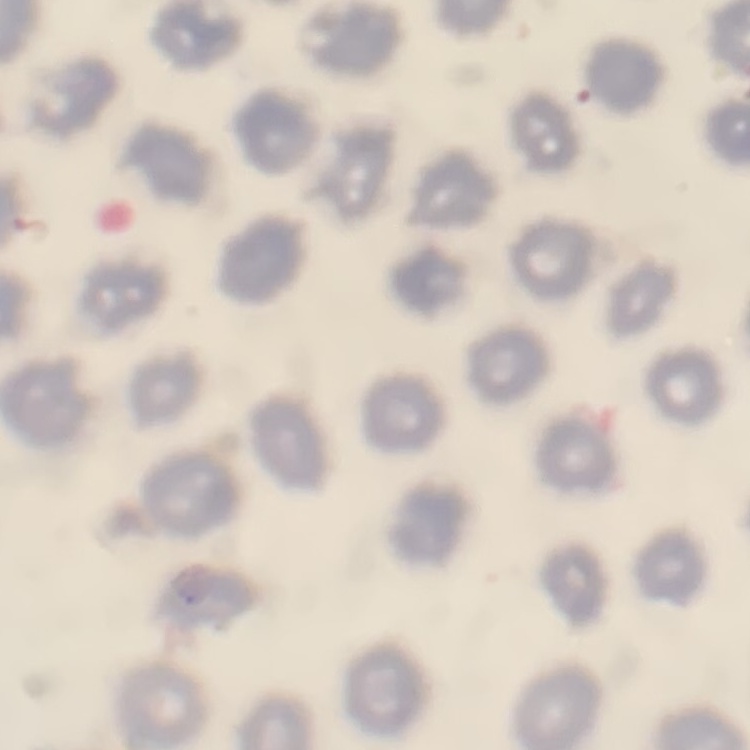
Summary:
  - Red blood cell morphology: no rouleaux formation
  - Image type: square crop of a larger photomicrograph
  - Stain: Field's or Giemsa
  - Preparation: thin blood smear